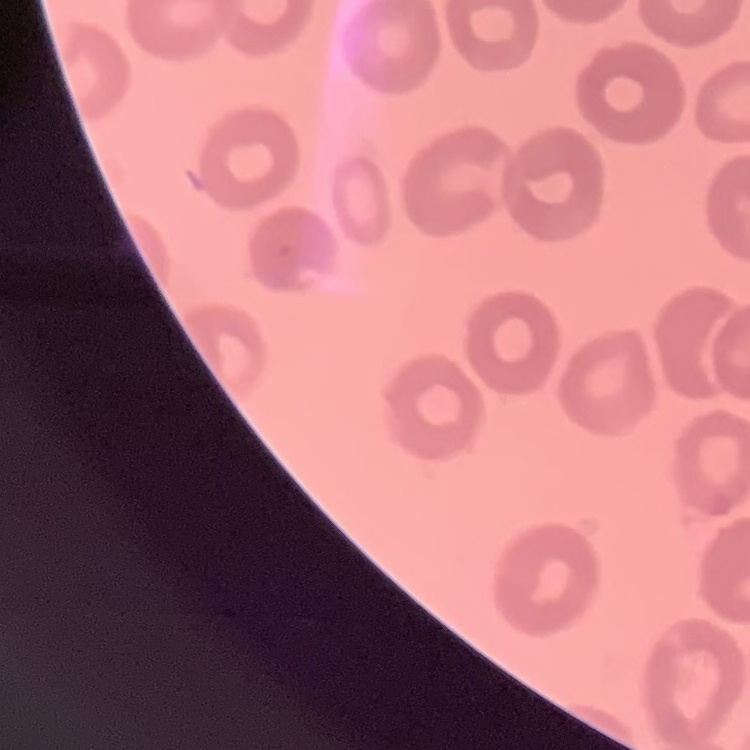
erythrocyte_morphology: no rouleaux formation
preparation: thin peripheral smear
stain: Field's or Giemsa
image_type: square crop of a larger photomicrograph